State which parasite is depicted.
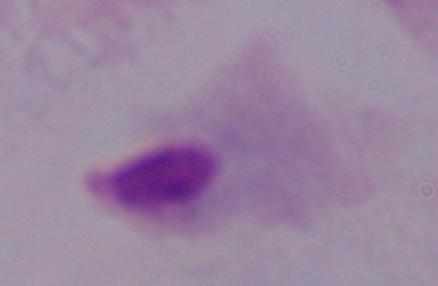

This is a trichomonad.

Captured at 1000x magnification. Photomicrograph.